Assess for Plasmodium parasites.
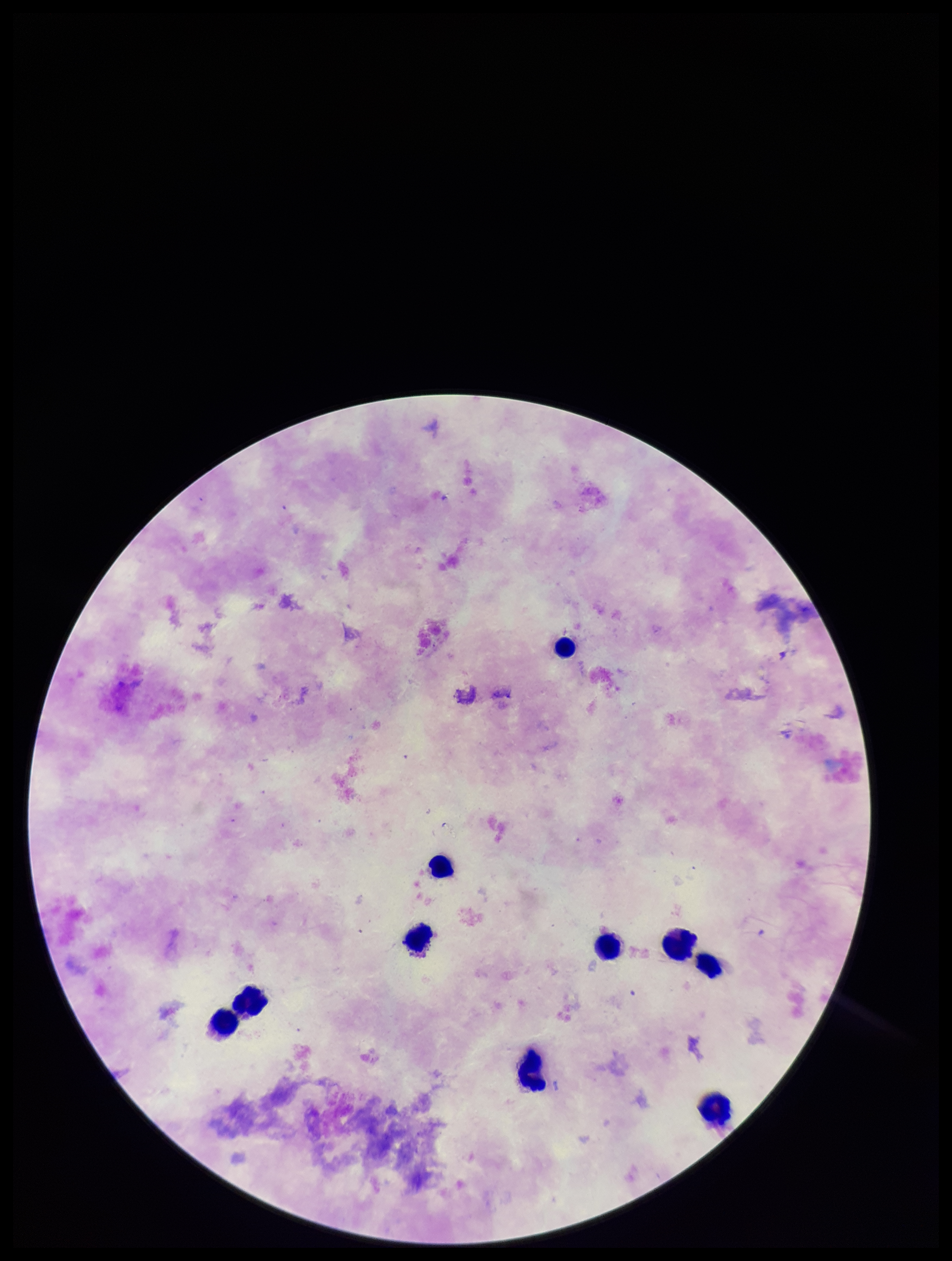
None identified.

{
  "capture": "smartphone photograph through the microscope eyepiece",
  "leukocyte_count": 10,
  "patient_malaria_status": "negative",
  "field_of_view": "single",
  "parasite_count": 0,
  "image_size": "952×1261 pixels",
  "stain": "Giemsa",
  "preparation": "thick"
}